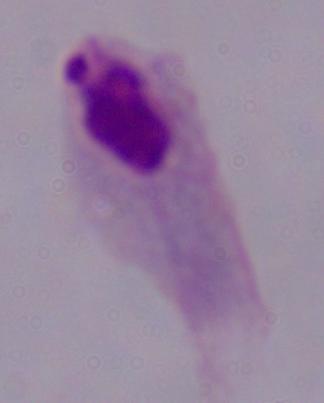
Summary:
  - Magnification: 1000x
  - Modality: micrograph
  - Identification: trichomonad